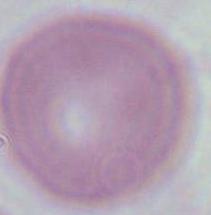

Summary:
  - Modality: micrograph
  - Magnification: 1000x
  - Identification: red blood cell